State which parasite is depicted.
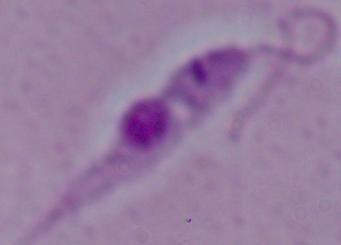

Leishmania.

modality: micrograph
magnification: 1000x